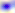
magnification: 400x
modality: micrograph
identification: Toxoplasma gondii